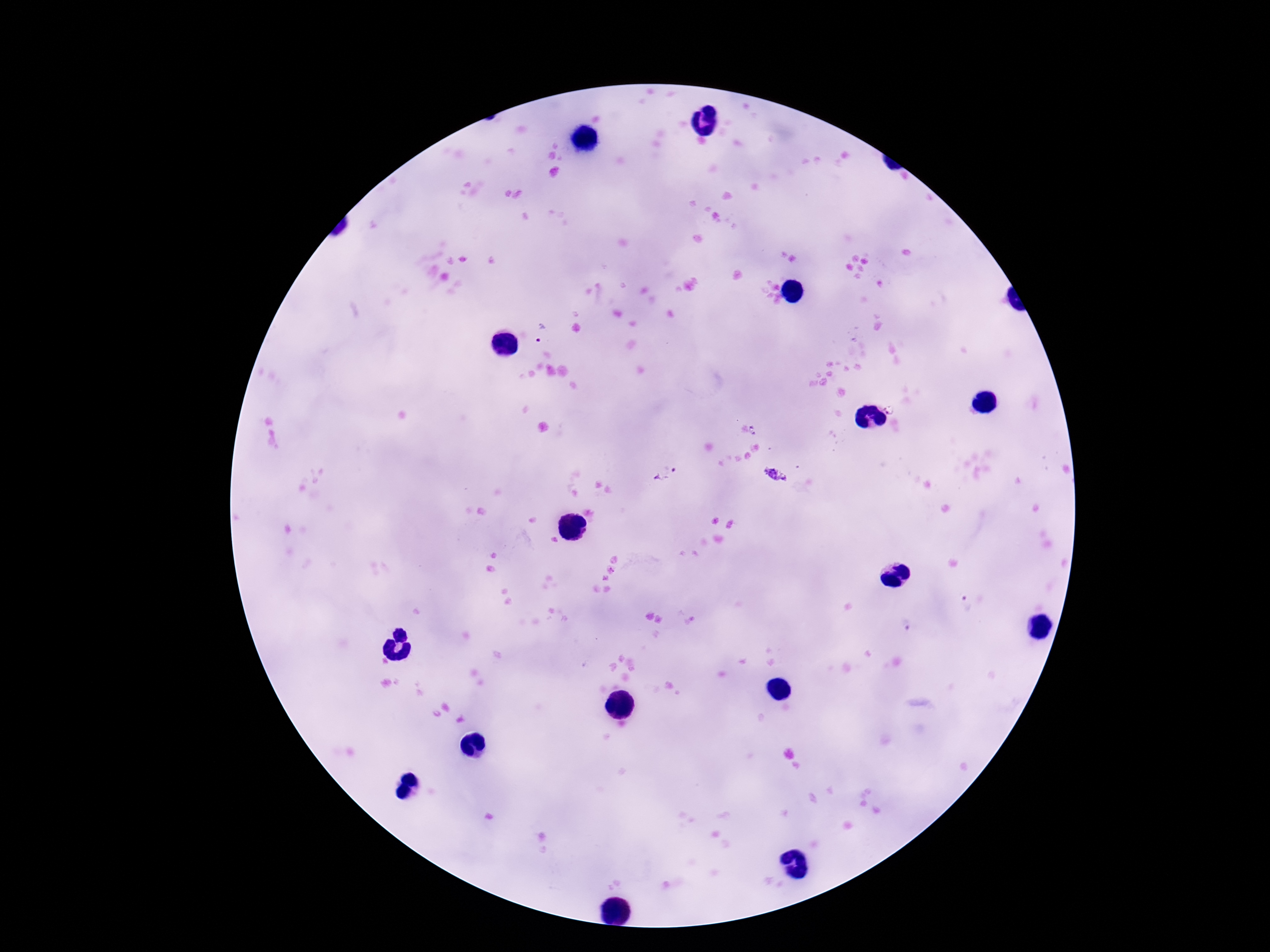
Approximate centers as {x, y} in pixels.
Summary:
  - Plasmodium parasite locations: {541, 333}, {889, 408}, {755, 430}, {666, 473}, {775, 475}, {965, 604}
  - Capture: smartphone camera through the microscope eyepiece
  - Patient malaria status: infected
  - Preparation: thick peripheral-blood smear
  - Field of view: one from this slide
  - Image size: 1270×952 pixels
  - Magnification: 100x
  - Stain: Giemsa